Give the extent of all Plasmodium vivax-infected red blood cells.
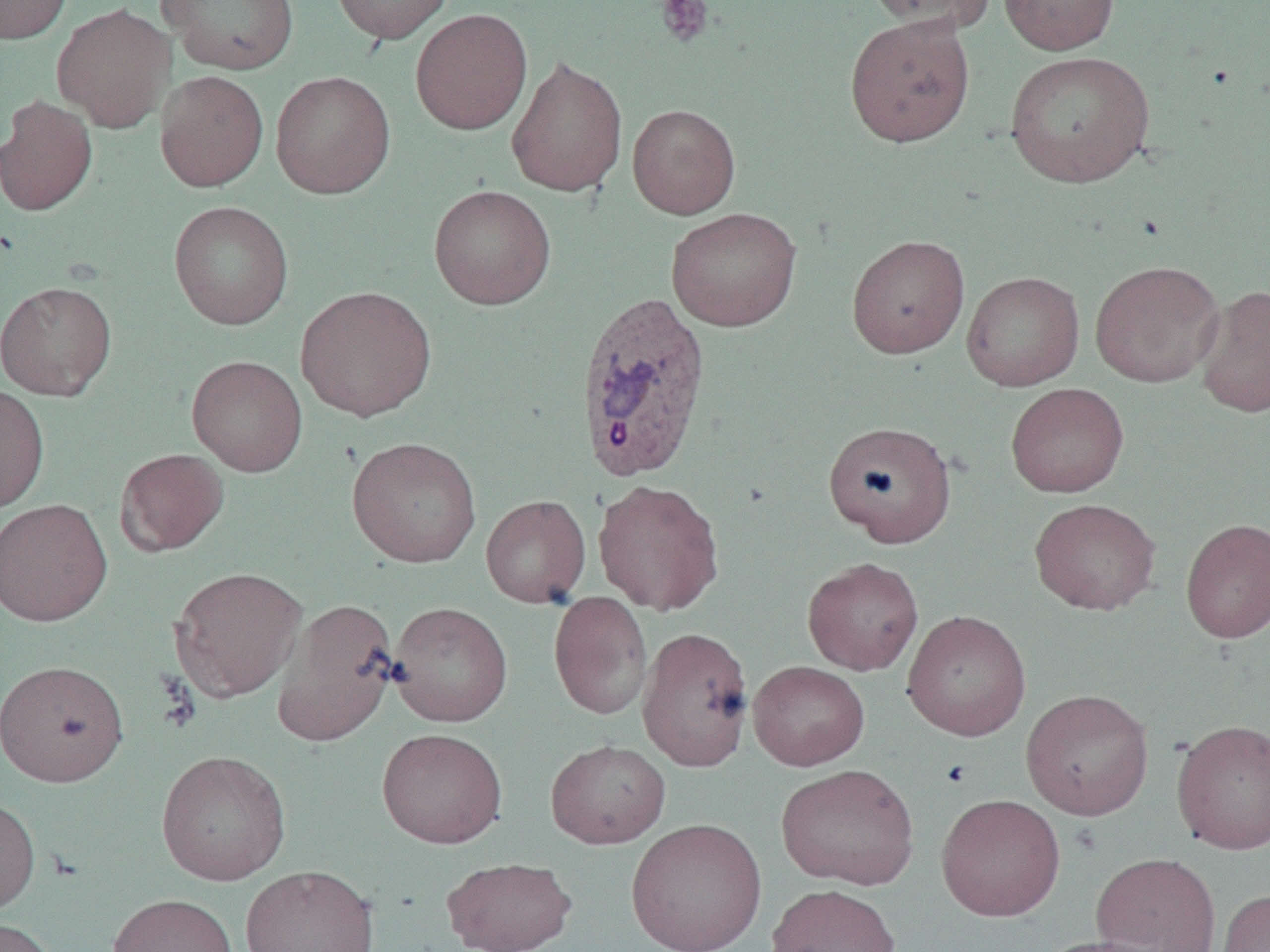
Approximate bounding boxes as (x1, y1, x2, y2) in pixels.
Plasmodium vivax-infected red blood cells: (574, 291, 713, 483).

Platelet locations: (655, 0, 714, 47). Uninfected red blood cell locations: (1, 0, 72, 44), (158, 0, 301, 75), (331, 0, 454, 44), (999, 0, 1120, 55), (863, 1, 998, 33), (51, 3, 174, 132), (409, 8, 532, 135), (844, 13, 976, 147), (1004, 50, 1156, 188), (506, 55, 628, 197), (155, 70, 269, 192), (271, 71, 395, 199), (0, 96, 98, 217), (628, 104, 740, 218), (429, 185, 556, 309), (168, 200, 294, 330), (666, 207, 802, 332), (846, 234, 969, 359), (1089, 259, 1225, 387), (962, 271, 1084, 391), (0, 280, 117, 400), (1195, 284, 1270, 418), (294, 285, 437, 422), (186, 355, 308, 476), (0, 383, 50, 514), (1006, 383, 1129, 497), (822, 420, 956, 546), (346, 436, 482, 568), (115, 448, 230, 556), (592, 479, 725, 616), (480, 495, 591, 608), (1029, 497, 1161, 615), (0, 498, 113, 626), (1180, 518, 1270, 643), (802, 556, 923, 675), (168, 566, 307, 701), (548, 591, 653, 720), (272, 597, 400, 746), (387, 601, 513, 727), (902, 610, 1032, 741), (636, 626, 755, 771), (0, 659, 130, 787), (748, 660, 870, 770), (1020, 689, 1154, 820), (1170, 718, 1270, 855), (376, 727, 508, 848), (545, 738, 671, 848), (156, 749, 291, 885), (776, 763, 919, 889), (935, 793, 1065, 920), (0, 794, 40, 917), (626, 816, 768, 952), (1091, 851, 1221, 952), (441, 856, 577, 952), (239, 863, 380, 952), (766, 883, 901, 952), (1216, 889, 1270, 952), (107, 892, 239, 952), (0, 918, 59, 952), (1035, 935, 1174, 952). Slide-level diagnosis: Plasmodium vivax. Thin blood smear. Image is 1270×952 pixels. 1000x magnification. Optical microscopy. One field of a larger specimen.